Comment on the morphology of the erythrocytes.
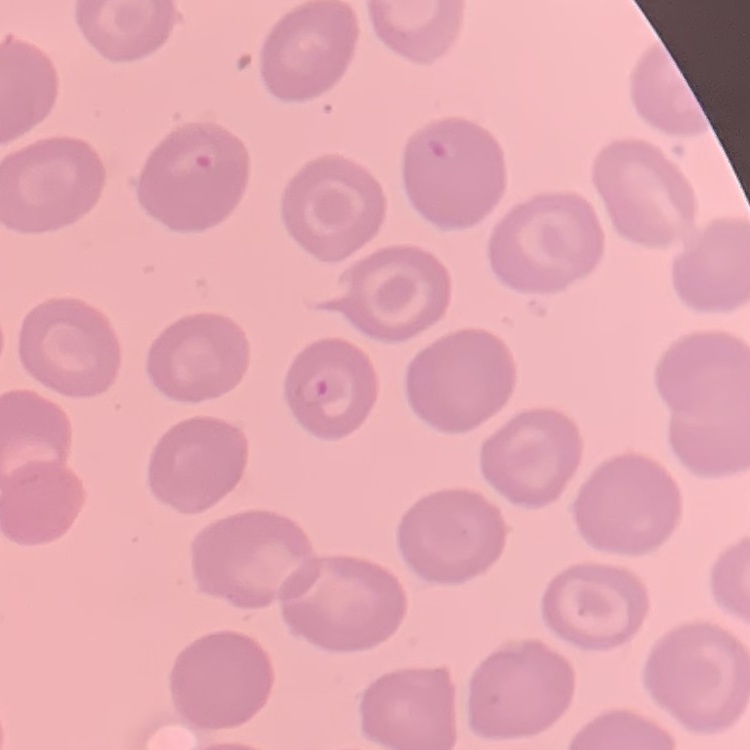
They show no rouleaux formation.

image type = square crop of a larger photomicrograph
stain = Field's or Giemsa
preparation = thin peripheral smear